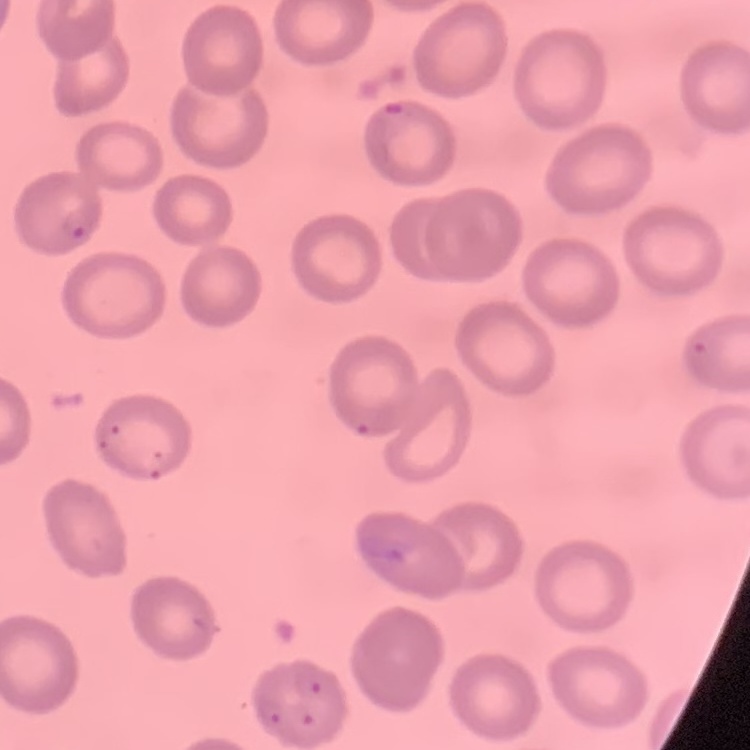
The red blood cells show no rouleaux formation. Square crop of a larger photomicrograph. Stained with either Field's or Giemsa. Thin blood smear.